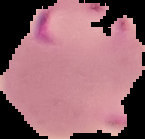 Image is 145×139 pixels. From a thin blood smear. Segmented cell region on a black background. Result: malaria parasites identified.